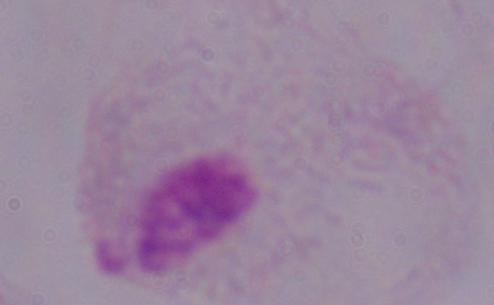

A trichomonad is seen. Photomicrograph. Captured at 1000x magnification.